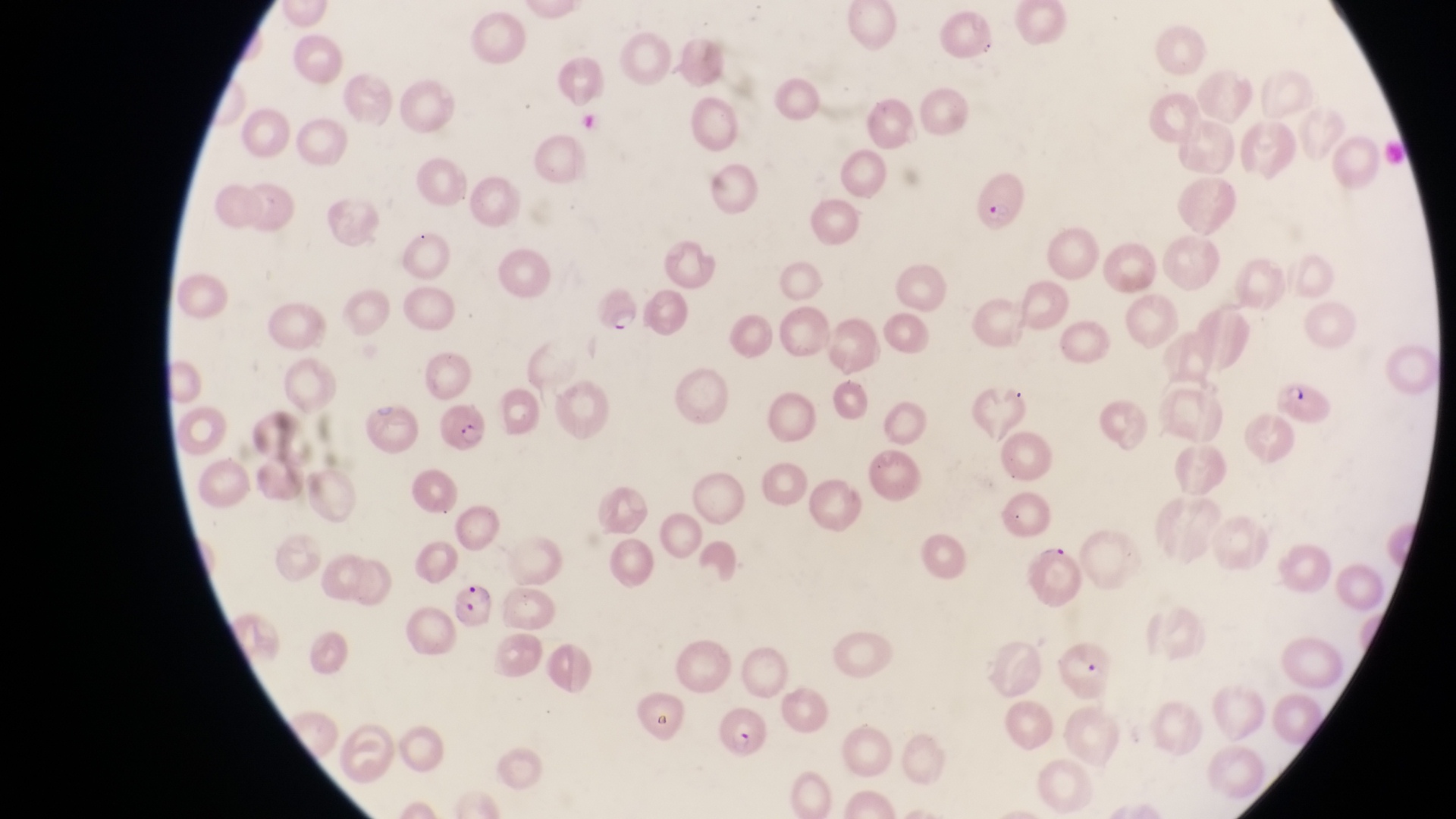

Approximate bounding boxes as [left, top, right, bottom] in pixels. Parasitised red blood cell locations: [968, 166, 1026, 229], [594, 287, 641, 336], [1274, 373, 1333, 423], [438, 400, 494, 455], [1036, 538, 1088, 611], [447, 582, 500, 632], [721, 703, 771, 758]. Sample from Uganda. One field of view. Thin blood film. At a magnification of 1000x. Image is 1456×819 pixels. Captured by a smartphone held over the eyepiece of an Olympus CX-23 microscope.